Assess this cell for malaria.
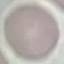
It is uninfected.

Giemsa-stained preparation. Cell patch, automatically extracted from a larger field of view and resized to 64 × 64 pixels. Thin blood smear. Photographed with a smartphone camera at the microscope eyepiece.